Outline each Plasmodium falciparum-infected red blood cell.
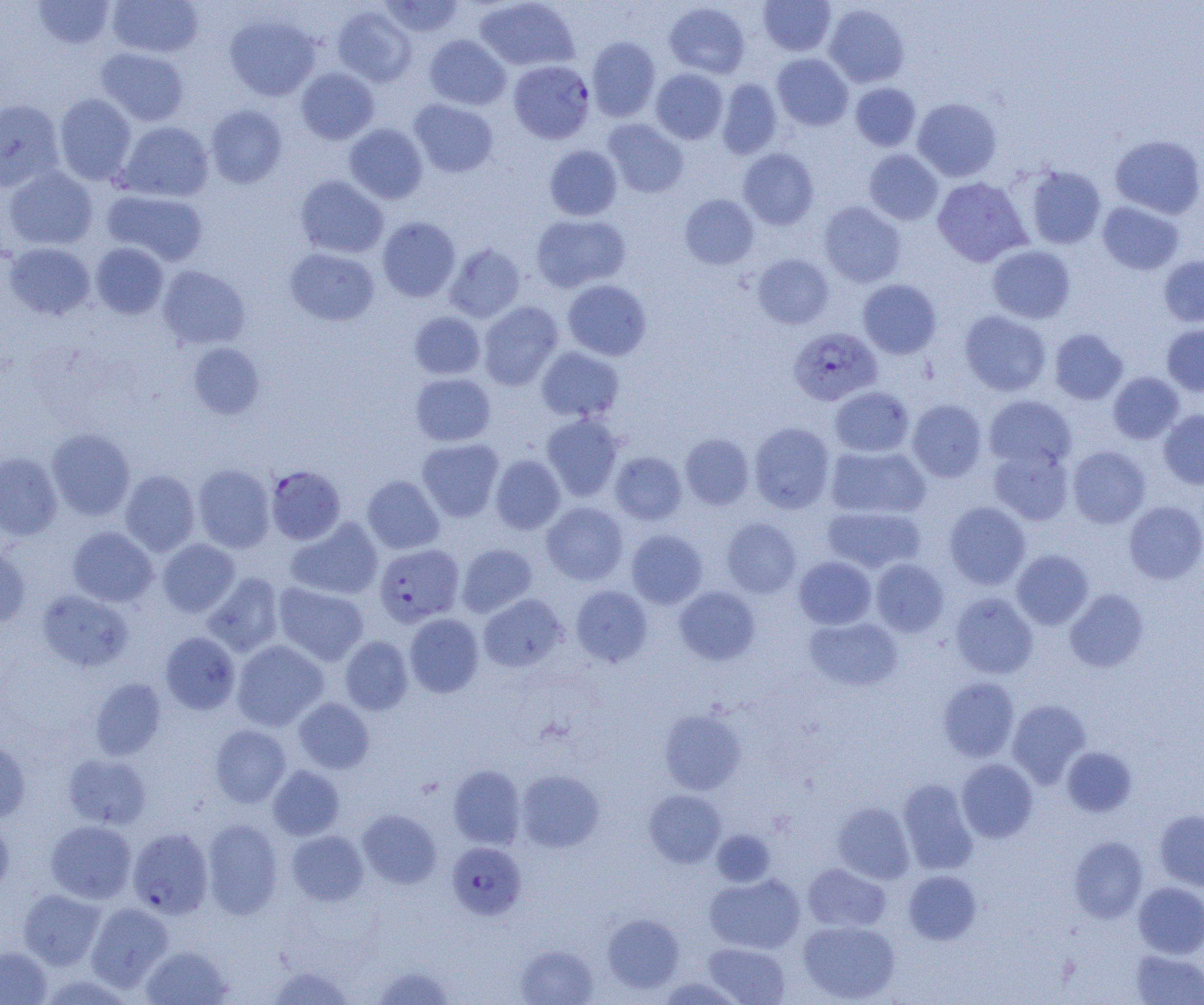
Approximate bounding boxes as (x1,y1)-(x2,y2) corner pairs in pixels.
Plasmodium falciparum-infected red blood cells (subset): (788,326)-(882,406), (266,465)-(345,545), (374,543)-(464,627), (127,827)-(214,918), (447,842)-(526,919).

slide-level diagnosis = Plasmodium falciparum
magnification = 1000x
preparation = thin blood film
field of view = single
modality = light microscopy
image size = 1204×1005 pixels
uninfected red blood cell locations (subset) = approximate bounding boxes as (x1,y1)-(x2,y2) corner pairs in pixels: (33,0)-(116,49), (107,0)-(204,58), (378,0)-(465,38), (474,0)-(580,72), (758,0)-(836,56), (664,2)-(751,79), (824,3)-(909,88), (332,5)-(417,87), (224,14)-(321,101), (424,34)-(511,110), (586,36)-(660,122), (96,47)-(189,126), (772,53)-(853,131), (296,67)-(379,144), (651,68)-(728,144), (716,78)-(782,159), (851,82)-(921,151), (53,93)-(137,185), (912,98)-(1002,181), (0,99)-(64,191), (409,99)-(499,177), (205,104)-(287,188), (603,119)-(688,197), (116,121)-(214,202), (344,123)-(428,204), (1110,134)-(1204,219), (544,144)-(622,221), (738,148)-(819,230), (864,149)-(943,225), (1023,165)-(1106,249), (3,166)-(98,250), (294,175)-(389,259), (932,177)-(1031,266), (102,190)-(208,266), (680,194)-(759,269), (819,201)-(906,287), (1097,201)-(1184,275), (530,213)-(631,292), (377,216)-(461,302), (3,242)-(95,320), (91,242)-(169,319), (443,243)-(526,323), (986,245)-(1076,324), (284,247)-(380,326), (752,253)-(834,329), (1159,255)-(1204,327), (157,265)-(250,350), (562,279)-(652,361), (858,279)-(941,358), (479,301)-(563,390), (959,310)-(1052,396), (409,312)-(485,379), (1161,324)-(1204,396), (1049,328)-(1128,405), (188,343)-(265,419), (536,346)-(625,422), (1108,372)-(1184,444), (410,373)-(496,446), (829,386)-(914,457), (983,395)-(1077,470), (907,399)-(987,482), (1158,409)-(1204,489), (541,412)-(623,501), (749,422)-(835,513), (47,427)-(135,520), (680,433)-(754,510), (416,438)-(504,522), (825,445)-(930,519), (1068,445)-(1150,528), (988,446)-(1073,525), (610,451)-(687,525), (0,452)-(63,540), (490,454)-(565,534), (193,464)-(275,553), (120,469)-(200,556), (362,475)-(444,554), (1124,500)-(1204,584), (944,501)-(1030,590), (541,502)-(628,585), (822,506)-(925,574), (286,516)-(383,600), (721,517)-(802,598), (67,527)-(158,606), (626,529)-(707,608), (157,539)-(240,618), (456,543)-(537,617), (0,546)-(31,628), (1012,549)-(1093,630), (794,556)-(877,629), (871,558)-(949,637), (201,572)-(284,657), (273,583)-(369,665), (571,585)-(653,667), (674,586)-(760,665), (1065,588)-(1149,672), (37,590)-(133,671), (950,592)-(1038,678), (478,594)-(567,672), (404,613)-(483,698), (804,616)-(903,692), (160,632)-(240,714), (340,636)-(413,715), (232,640)-(328,731), (937,677)-(1019,762), (90,678)-(167,760), (293,697)-(374,773), (1007,699)-(1091,788), (659,708)-(747,795), (210,725)-(291,807), (0,739)-(31,823), (1062,747)-(1137,817), (63,753)-(152,830), (956,758)-(1038,843), (268,765)-(344,840), (448,765)-(526,849), (516,769)-(604,852), (898,778)-(979,875), (644,789)-(727,867), (832,801)-(915,884), (1154,809)-(1204,891), (357,810)-(441,889), (0,817)-(14,899), (202,818)-(283,919), (45,820)-(137,903), (287,830)-(368,906), (711,830)-(775,887), (1069,836)-(1148,923), (802,863)-(891,933), (903,870)-(981,945), (704,873)-(805,954), (1134,882)-(1204,958), (18,888)-(105,970), (85,902)-(173,991), (602,913)-(685,993), (798,920)-(900,1004), (703,942)-(791,1005), (514,944)-(599,1005), (0,945)-(52,1004), (140,945)-(233,1004), (1131,949)-(1204,1004), (267,964)-(355,1005), (371,964)-(457,1004), (657,977)-(745,1005)